Assess the morphology of the red blood cells.
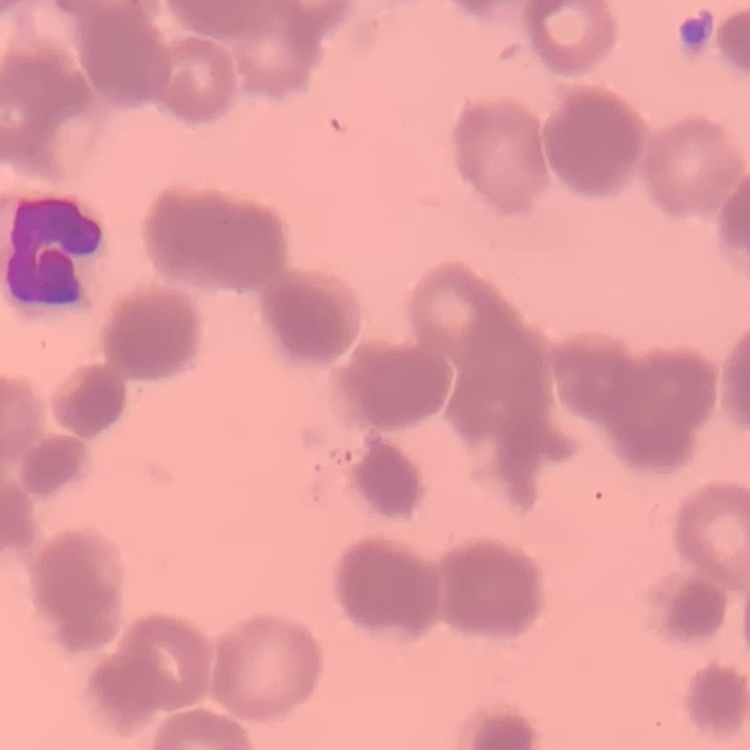
They show rouleaux formation.

Thin blood film. One tile cut from a larger photomicrograph. Stained with either Field's or Giemsa.